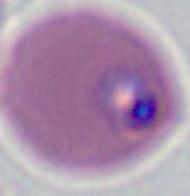

Micrograph. A Plasmodium parasite is shown. Captured at either 400x or 1000x magnification.